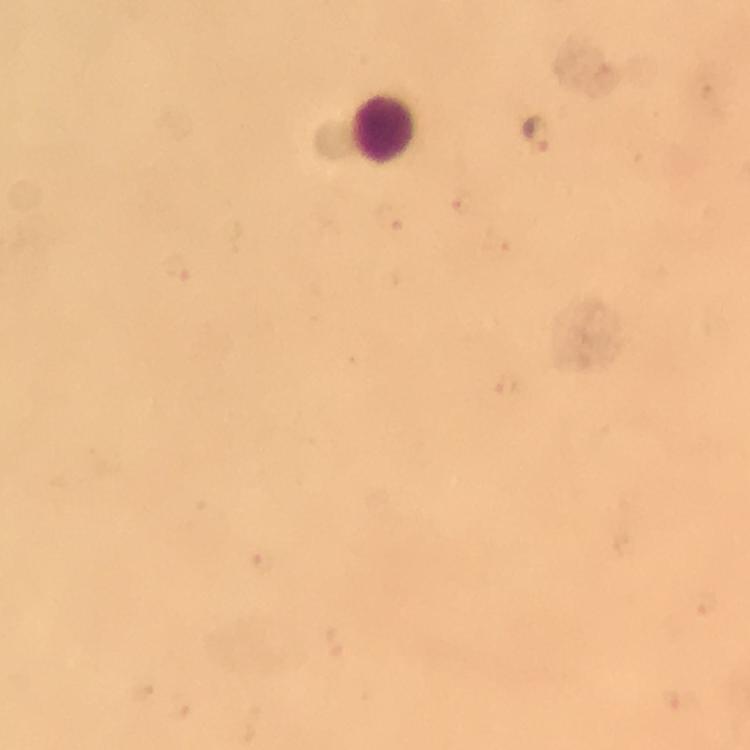
Approximate object centers, in pixels from the top-left corner.
Summary:
  - Leukocyte locations: (x=383, y=129)
  - Plasmodium parasite locations: (x=538, y=133)
  - Cropped from: one field of view
  - Magnification: 100x
  - Capture: smartphone camera through the microscope
  - Context: from a malaria diagnostic workup
  - Immersion oil: used
  - Stain: Giemsa
  - Image size: 750×750 pixels
  - Preparation: thick blood smear